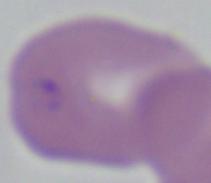

Summary:
  - Magnification: 1000x
  - Identification: Babesia
  - Modality: micrograph